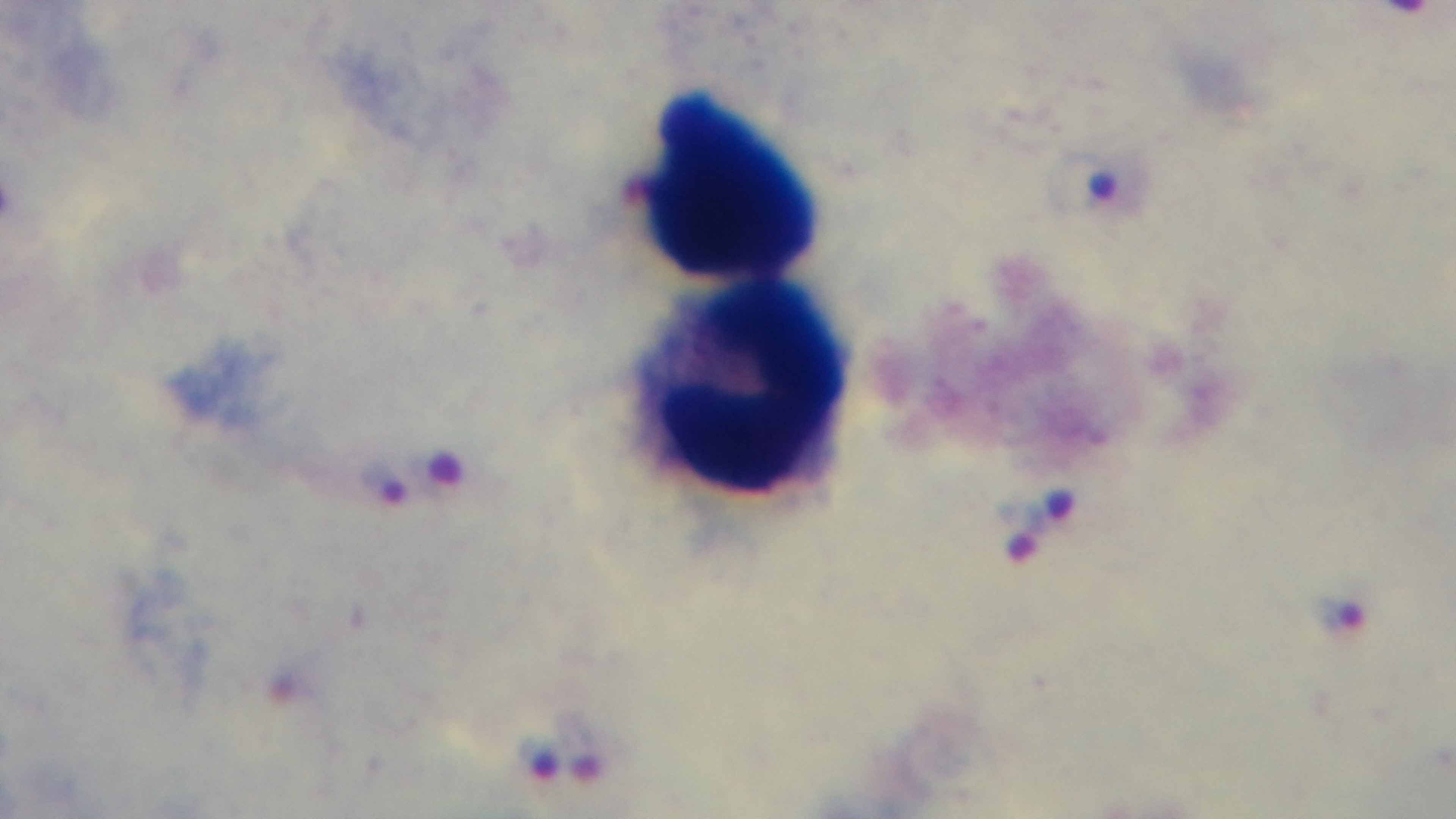

field of view = one from the slide
preparation = thick smear
capture = mounted 4K digital camera
objective = 100x oil immersion
stain = Giemsa
malaria status = positive
modality = light microscopy